Give the preparation type.
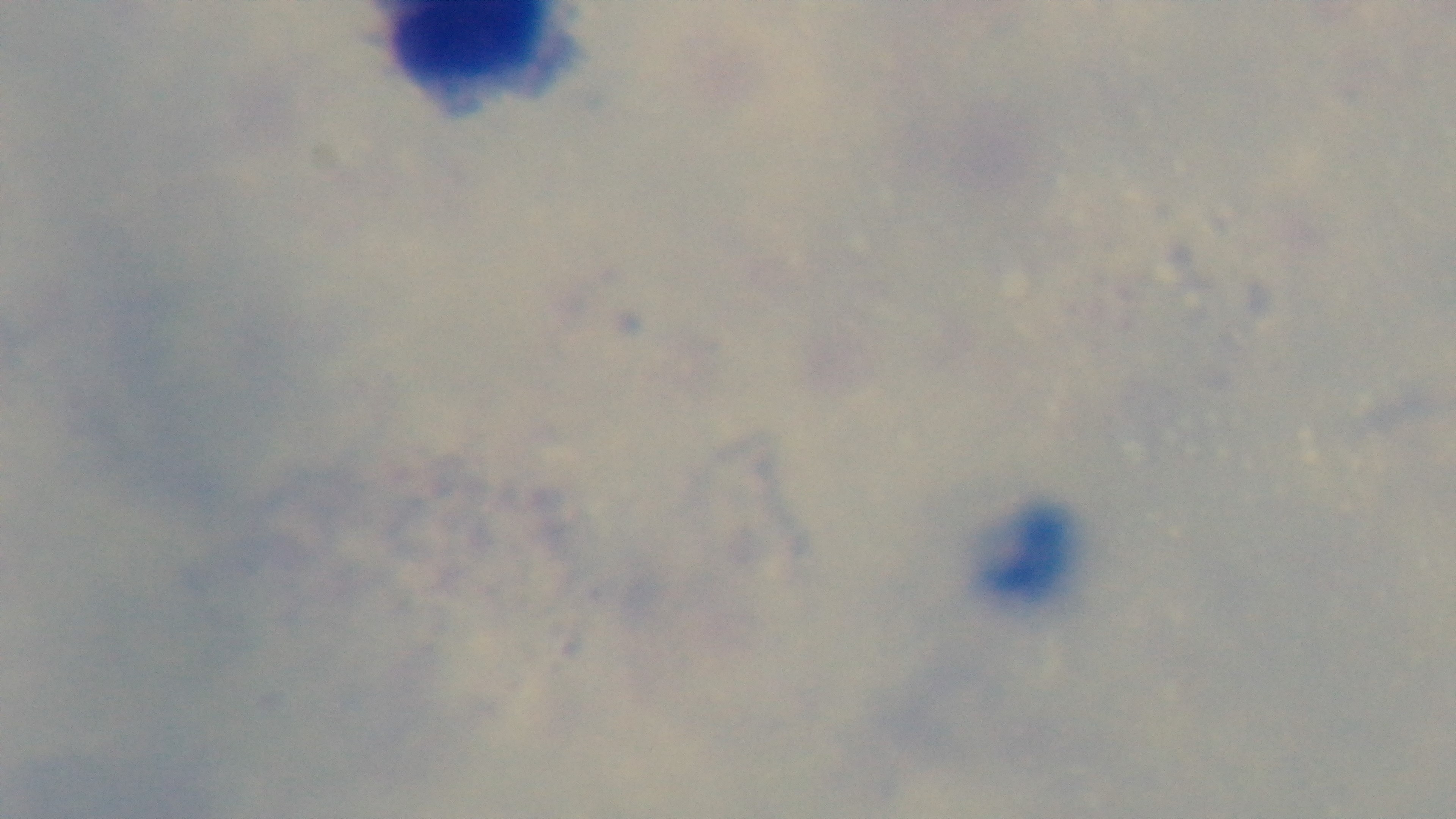
It is a thick blood film.

Giemsa-stained. Photomicrograph. 100x oil-immersion objective. Malaria status: uninfected. Single field of view. Mounted 4K digital camera.